Comment on the morphology of the red blood cells.
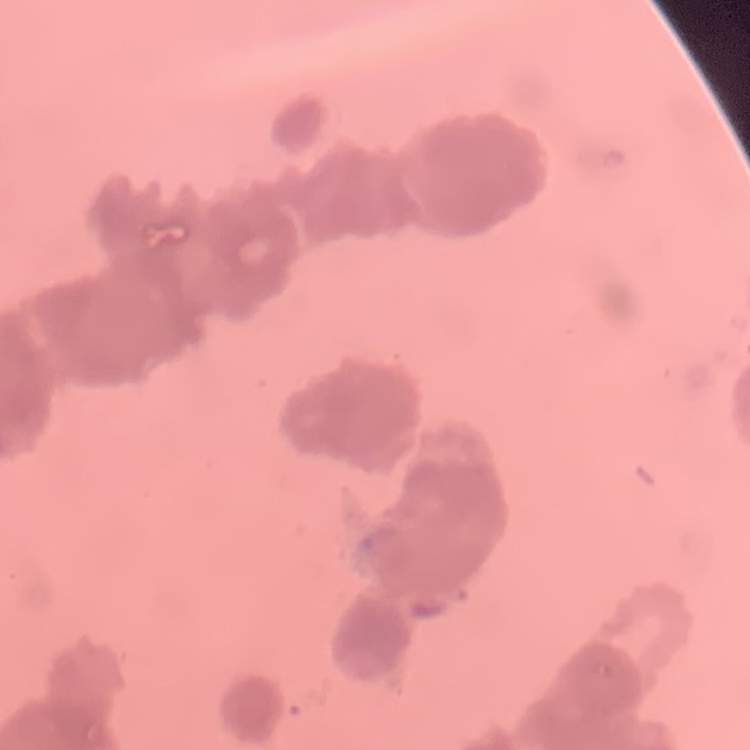

Rouleaux formation.

{
  "preparation": "thin peripheral smear",
  "stain": "Field's or Giemsa",
  "image_type": "one tile cut from a larger photomicrograph"
}